Assess the morphology of the erythrocytes.
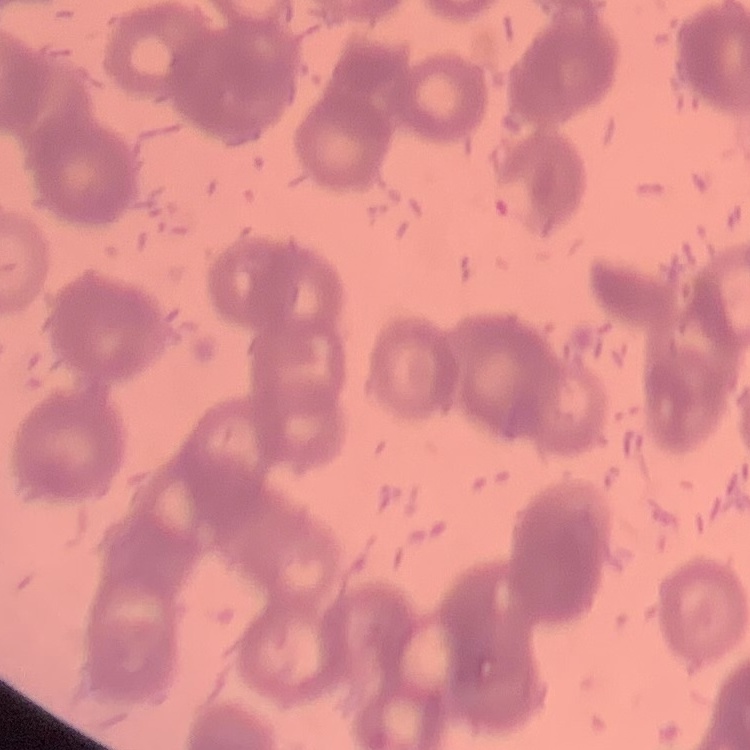

They show rouleaux formation.

Stained with either Field's or Giemsa. Thin peripheral smear. One tile cut from a larger photomicrograph.